State which parasite is depicted.
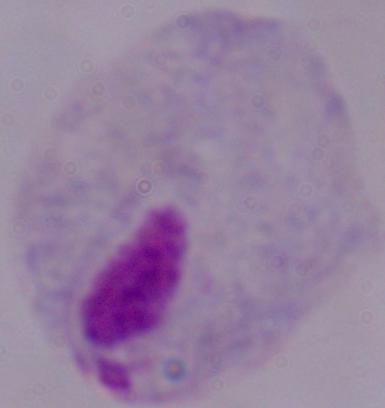

This is a trichomonad.

Summary:
  - Magnification: 1000x
  - Modality: photomicrograph